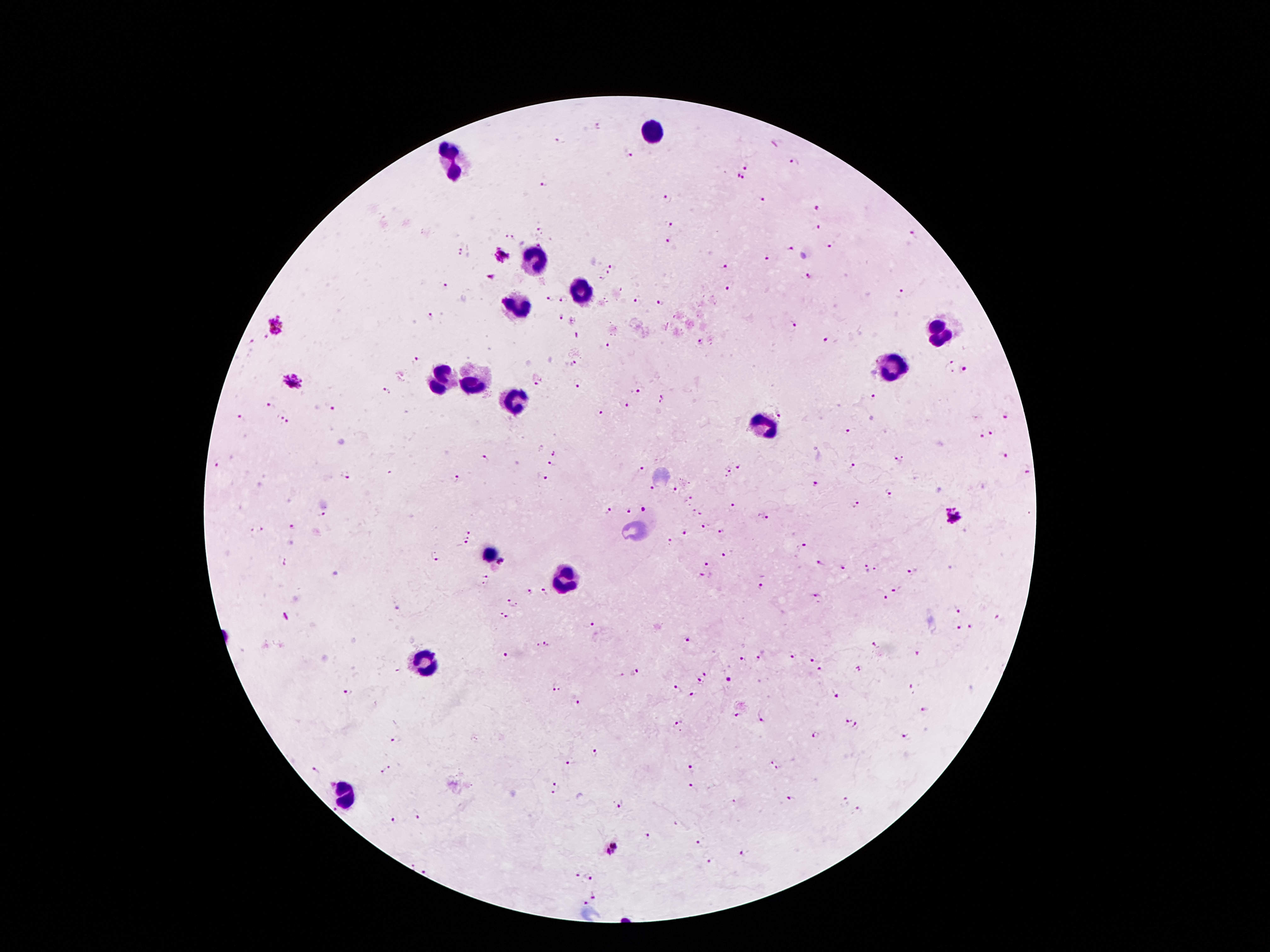

Approximate centers as [x, y] in pixels.
Summary:
  - Leukocyte locations: [653, 131], [454, 159], [535, 259], [579, 289], [515, 308], [937, 332], [895, 365], [441, 379], [472, 381], [515, 405], [765, 428], [487, 555], [559, 578], [426, 663], [349, 795]
  - Plasmodium parasite locations: [599, 126], [558, 142], [629, 156], [793, 163], [747, 166], [739, 179], [543, 185], [665, 199], [760, 199], [816, 208], [671, 225], [818, 228], [540, 229], [914, 234], [509, 236], [667, 239], [541, 243], [830, 246], [790, 249], [459, 252], [501, 256], [766, 258], [726, 266], [612, 267], [608, 274], [808, 276], [600, 278], [446, 287], [727, 287], [901, 293], [549, 298], [565, 300], [637, 301], [661, 301], [431, 315], [560, 316], [794, 325], [276, 327], [264, 338], [825, 339], [701, 341], [251, 342], [608, 346], [416, 361], [950, 362], [572, 364], [964, 368], [292, 382], [537, 384], [578, 384], [640, 389], [385, 391], [872, 397], [661, 399], [627, 405], [267, 406], [333, 409], [780, 413], [601, 414], [241, 417], [1004, 418], [284, 419], [848, 432], [993, 434], [981, 435], [556, 453], [1003, 456], [485, 458], [899, 458], [218, 464], [553, 466], [739, 466], [855, 466], [641, 470], [727, 470], [349, 475], [458, 478], [545, 480], [816, 483], [651, 488], [675, 489], [889, 491], [692, 497], [857, 504], [731, 506], [645, 510], [693, 510], [610, 511], [627, 512], [322, 514], [702, 514], [764, 516], [952, 516], [704, 524], [291, 528], [262, 529], [721, 530], [250, 531], [469, 531], [685, 533], [468, 538], [669, 541], [464, 544], [805, 544], [727, 555], [435, 557], [501, 561], [708, 564], [822, 564], [843, 567], [878, 568], [866, 569], [912, 572], [703, 575], [485, 577], [760, 587], [530, 591], [894, 591], [544, 592], [816, 597], [886, 597], [512, 604], [958, 612], [503, 617], [999, 619], [593, 623], [972, 625], [958, 627], [688, 638], [874, 644], [542, 645], [917, 654], [792, 655], [505, 656], [743, 658], [759, 658], [811, 661], [859, 668], [822, 670], [636, 672], [706, 672], [728, 679], [700, 680], [556, 688], [913, 688], [677, 689], [347, 691], [693, 695], [835, 696], [577, 704], [925, 711], [737, 715], [762, 718], [846, 719], [677, 725], [857, 727], [814, 735], [905, 736], [396, 739], [596, 752], [772, 762], [570, 763], [390, 767], [693, 768], [780, 769], [315, 770], [382, 772], [555, 783], [691, 786], [554, 795], [789, 798], [734, 801], [843, 801], [623, 804], [336, 810], [859, 811], [417, 816], [395, 820], [675, 825], [647, 836], [698, 842], [612, 849], [743, 853], [710, 860], [429, 870], [578, 877], [592, 877], [594, 895], [584, 904]
  - Field of view: single
  - Stain: Giemsa
  - Preparation: thick blood film
  - Magnification: 100x
  - Capture: smartphone through the microscope eyepiece
  - Image size: 1270×952 pixels
  - Patient malaria status: positive for Plasmodium falciparum